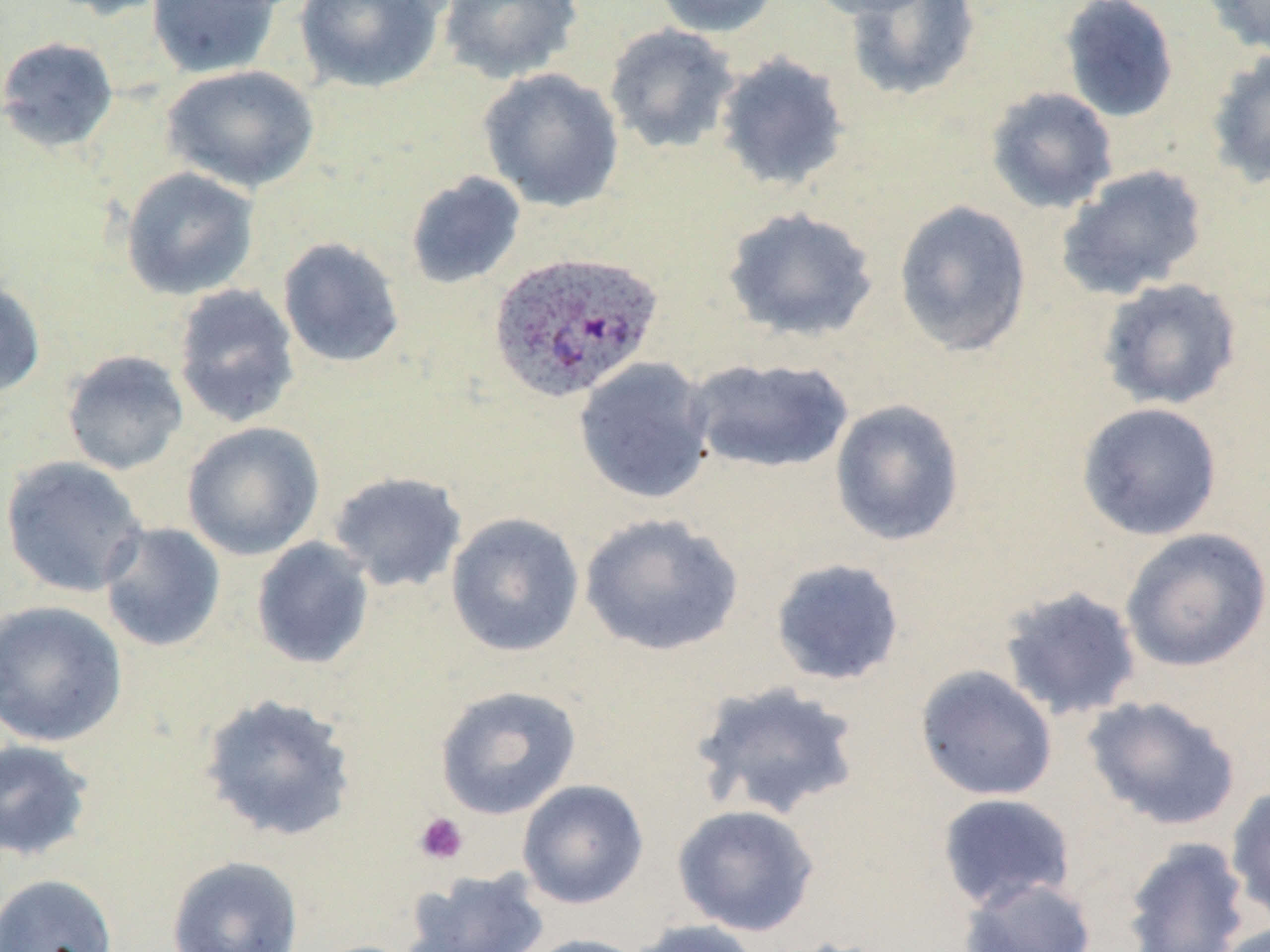
Plasmodium ovale-infected red blood cell locations = approximate bounding boxes as [x1, y1, x2, y2] in pixels: [488, 250, 662, 403]
slide-level diagnosis = Plasmodium ovale
preparation = thin blood film
uninfected red blood cell locations = approximate bounding boxes as [x1, y1, x2, y2] in pixels: [41, 0, 178, 20], [146, 0, 282, 79], [293, 0, 447, 94], [438, 0, 583, 84], [651, 0, 782, 38], [801, 0, 944, 20], [1059, 0, 1179, 123], [1202, 0, 1270, 57], [842, 1, 981, 102], [603, 23, 741, 155], [0, 36, 119, 153], [1205, 48, 1270, 190], [713, 52, 851, 193], [161, 65, 320, 193], [477, 68, 624, 212], [984, 87, 1118, 214], [1056, 164, 1209, 301], [120, 166, 260, 301], [405, 171, 526, 290], [893, 199, 1033, 357], [721, 205, 879, 343], [277, 236, 406, 369], [1098, 277, 1242, 411], [0, 278, 46, 400], [171, 283, 301, 429], [60, 350, 190, 475], [573, 357, 716, 504], [686, 357, 854, 475], [829, 399, 965, 547], [1076, 402, 1223, 541], [182, 422, 325, 560], [0, 456, 149, 598], [327, 471, 468, 593], [445, 512, 585, 657], [579, 513, 744, 657], [98, 522, 227, 653], [1120, 528, 1270, 672], [250, 537, 375, 670], [769, 557, 905, 687], [998, 585, 1143, 722], [0, 600, 128, 748], [915, 665, 1058, 802], [691, 679, 864, 821], [434, 684, 582, 819], [198, 692, 359, 843], [1082, 695, 1242, 832], [0, 739, 96, 862], [517, 779, 648, 909], [1225, 785, 1270, 924], [936, 792, 1076, 912], [671, 804, 821, 937], [1121, 837, 1252, 952], [166, 855, 304, 952], [404, 867, 551, 952], [0, 873, 118, 952], [958, 875, 1098, 952], [628, 919, 767, 952], [1215, 921, 1269, 952], [519, 934, 651, 952], [782, 936, 905, 952]
field of view = single
modality = light microscopy
platelet locations = approximate bounding boxes as [x1, y1, x2, y2] in pixels: [413, 812, 469, 865]
magnification = 1000x
image size = 1270×952 pixels
stain = May-Grünwald-Giemsa